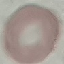
result: no malaria parasites seen
capture: smartphone through the microscope eyepiece
preparation: thin blood smear
image_type: cell patch, automatically extracted from a larger field of view and resized to 64 × 64 pixels
stain: Giemsa